Assess this cell for malaria.
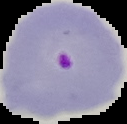

Parasitized.

The area outside the segmented cell region is set to black. From a thin blood film. Image is 127×124 pixels.